Name the parasite shown.
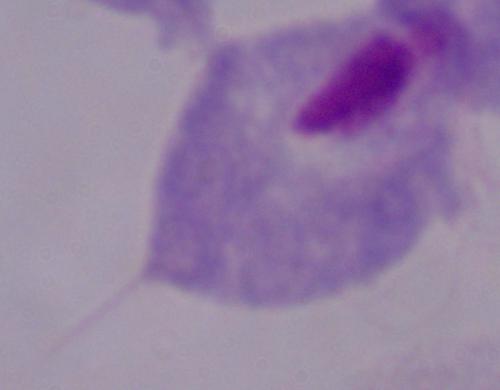

A trichomonad.

Summary:
  - Magnification: 1000x
  - Modality: photomicrograph